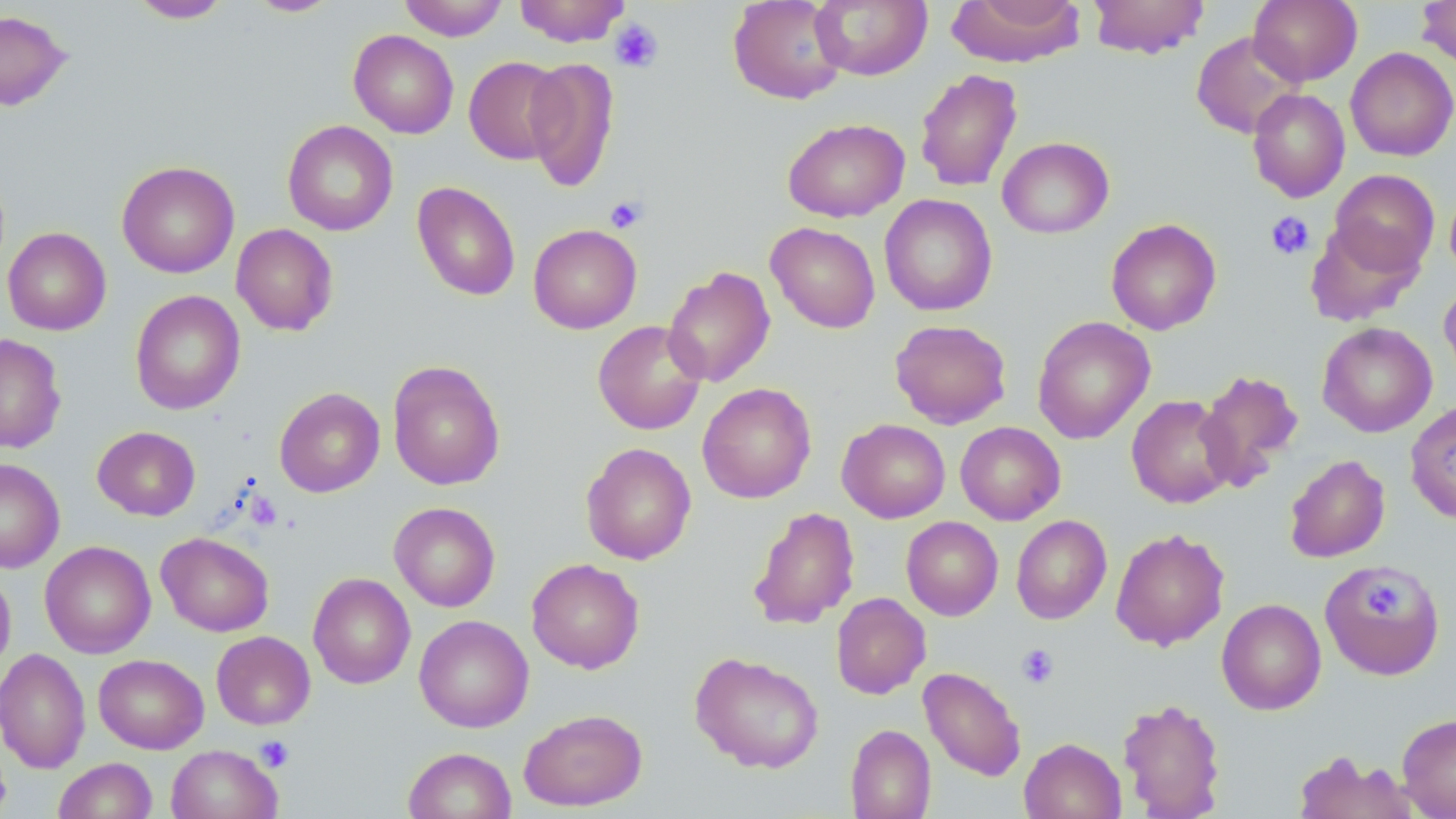
slide_level_diagnosis: negative for blood parasites
modality: optical microscopy
uninfected_red_blood_cell_locations: 'approximate bounding boxes as named x1/y1/x2/y2 corners in pixels: (x1=128, y1=0, x2=233, y2=23), (x1=398, y1=0, x2=509, y2=41), (x1=514, y1=0, x2=631, y2=47), (x1=728, y1=0, x2=848, y2=105), (x1=810, y1=0, x2=932, y2=81), (x1=948, y1=0, x2=1086, y2=67), (x1=1088, y1=0, x2=1210, y2=59), (x1=1248, y1=0, x2=1362, y2=86), (x1=1417, y1=0, x2=1456, y2=68), (x1=246, y1=1, x2=342, y2=17), (x1=0, y1=9, x2=71, y2=111), (x1=349, y1=30, x2=459, y2=139), (x1=1191, y1=31, x2=1305, y2=139), (x1=1345, y1=47, x2=1456, y2=161), (x1=464, y1=56, x2=566, y2=165), (x1=524, y1=56, x2=620, y2=192), (x1=914, y1=68, x2=1023, y2=192), (x1=1247, y1=88, x2=1350, y2=203), (x1=782, y1=118, x2=909, y2=222), (x1=283, y1=120, x2=398, y2=236), (x1=997, y1=137, x2=1114, y2=238), (x1=116, y1=160, x2=240, y2=278), (x1=1329, y1=169, x2=1439, y2=276), (x1=412, y1=181, x2=520, y2=301), (x1=1445, y1=184, x2=1456, y2=281), (x1=880, y1=194, x2=997, y2=316), (x1=1105, y1=218, x2=1222, y2=335), (x1=1305, y1=220, x2=1422, y2=326), (x1=766, y1=222, x2=880, y2=333), (x1=231, y1=223, x2=339, y2=336), (x1=528, y1=224, x2=642, y2=334), (x1=2, y1=227, x2=111, y2=335), (x1=663, y1=266, x2=776, y2=387), (x1=1439, y1=281, x2=1456, y2=387), (x1=130, y1=289, x2=245, y2=415), (x1=1032, y1=316, x2=1155, y2=444), (x1=889, y1=319, x2=1012, y2=429), (x1=592, y1=320, x2=708, y2=435), (x1=1317, y1=322, x2=1437, y2=437), (x1=0, y1=333, x2=67, y2=454), (x1=387, y1=359, x2=505, y2=491), (x1=1195, y1=369, x2=1304, y2=493), (x1=697, y1=383, x2=816, y2=504), (x1=274, y1=387, x2=385, y2=497), (x1=1126, y1=394, x2=1236, y2=508), (x1=1405, y1=401, x2=1456, y2=524), (x1=837, y1=419, x2=950, y2=523), (x1=955, y1=422, x2=1066, y2=525), (x1=92, y1=426, x2=200, y2=521), (x1=581, y1=442, x2=696, y2=565), (x1=1284, y1=454, x2=1390, y2=563), (x1=0, y1=458, x2=65, y2=573), (x1=389, y1=502, x2=501, y2=612), (x1=748, y1=506, x2=860, y2=629), (x1=1011, y1=515, x2=1111, y2=624), (x1=901, y1=516, x2=1003, y2=620), (x1=1111, y1=527, x2=1229, y2=650), (x1=156, y1=532, x2=274, y2=636), (x1=40, y1=541, x2=156, y2=659), (x1=526, y1=558, x2=645, y2=673), (x1=1318, y1=561, x2=1445, y2=680), (x1=0, y1=566, x2=16, y2=680), (x1=308, y1=572, x2=415, y2=689), (x1=830, y1=592, x2=931, y2=699), (x1=1216, y1=598, x2=1326, y2=715), (x1=414, y1=614, x2=534, y2=733), (x1=212, y1=631, x2=315, y2=729), (x1=0, y1=648, x2=91, y2=774), (x1=689, y1=652, x2=825, y2=773), (x1=93, y1=653, x2=209, y2=754), (x1=918, y1=666, x2=1026, y2=781), (x1=1117, y1=696, x2=1227, y2=818), (x1=518, y1=708, x2=647, y2=811), (x1=1397, y1=713, x2=1456, y2=818), (x1=845, y1=724, x2=935, y2=819), (x1=1019, y1=737, x2=1126, y2=819), (x1=166, y1=744, x2=282, y2=819), (x1=403, y1=747, x2=517, y2=819), (x1=1292, y1=751, x2=1416, y2=819), (x1=53, y1=758, x2=158, y2=819)'
stain: May-Grünwald-Giemsa
magnification: 1000x
field_of_view: single
platelet_locations: 'approximate bounding boxes as named x1/y1/x2/y2 corners in pixels: (x1=609, y1=19, x2=664, y2=73), (x1=604, y1=195, x2=648, y2=234), (x1=1265, y1=211, x2=1315, y2=260), (x1=1364, y1=582, x2=1400, y2=617), (x1=1017, y1=644, x2=1059, y2=688), (x1=255, y1=736, x2=294, y2=772)'
preparation: thin blood film
image_size: 1456×819 pixels